Name the parasite shown.
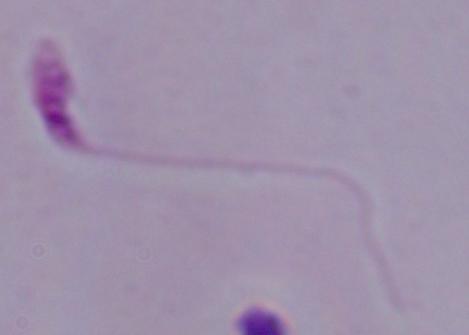

This is Leishmania.

1000x magnification. Photomicrograph.